Name the parasite shown.
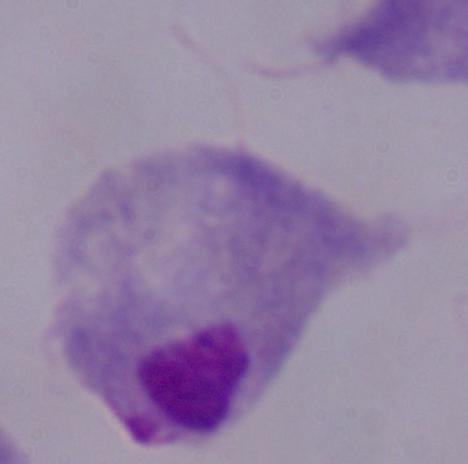
A trichomonad.

modality: micrograph
magnification: 1000x